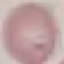
Summary:
  - Malaria status: uninfected
  - Capture: smartphone through the microscope eyepiece
  - Image type: cell patch, automatically extracted from a larger field of view and resized to 64 × 64 pixels
  - Preparation: thin blood smear
  - Stain: Giemsa